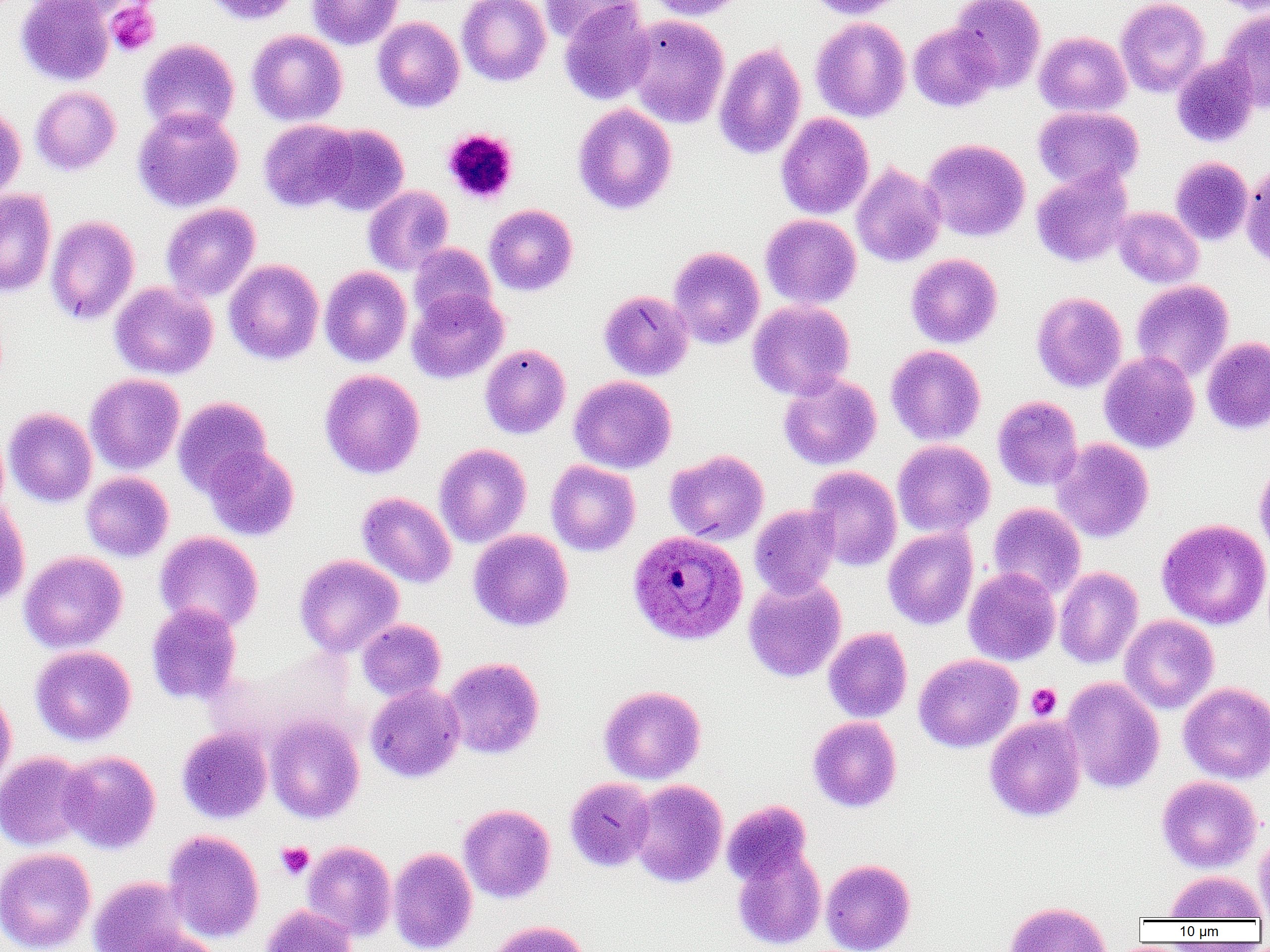 Approximate bounding boxes as (x1, y1, x2, y2) in pixels. Plasmodium ovale-infected red blood cell locations: (627, 529, 748, 645). Platelet locations (subset): (442, 128, 519, 204), (1026, 683, 1061, 720), (276, 842, 314, 879). Uninfected red blood cell locations (subset): (16, 0, 114, 86), (27, 0, 141, 22), (200, 0, 301, 25), (307, 0, 403, 50), (457, 0, 551, 86), (541, 0, 638, 44), (643, 0, 748, 21), (806, 0, 908, 19), (949, 0, 1046, 92), (1115, 0, 1210, 97), (1209, 0, 1270, 14), (559, 1, 654, 106), (1217, 8, 1270, 111), (624, 14, 729, 128), (372, 17, 465, 112), (810, 17, 911, 122), (908, 23, 998, 112), (247, 29, 347, 126), (1034, 31, 1132, 117), (138, 38, 240, 135), (714, 43, 807, 160), (1171, 55, 1261, 148), (30, 86, 121, 176), (0, 103, 26, 202), (573, 103, 677, 215), (1033, 106, 1143, 192), (133, 107, 243, 212), (775, 113, 874, 219), (258, 119, 358, 212), (312, 123, 409, 215), (922, 139, 1030, 242), (1170, 156, 1253, 246), (1241, 161, 1270, 271), (851, 162, 946, 268), (1031, 167, 1133, 267), (363, 185, 454, 276), (0, 189, 56, 298), (161, 203, 260, 302), (484, 204, 578, 295), (1113, 207, 1203, 288), (760, 214, 862, 309), (45, 215, 140, 325), (408, 243, 497, 326), (668, 246, 765, 349), (906, 253, 1003, 348), (224, 259, 324, 365), (320, 266, 412, 366), (1131, 280, 1234, 381), (110, 282, 218, 379), (407, 289, 509, 384), (598, 290, 694, 381), (1031, 292, 1127, 393), (747, 300, 855, 400), (1202, 337, 1270, 434), (480, 343, 571, 439), (886, 345, 986, 445), (1099, 352, 1200, 453), (319, 369, 425, 479), (85, 373, 185, 475), (778, 373, 882, 470), (569, 375, 677, 473), (992, 395, 1083, 491), (173, 396, 273, 496), (3, 407, 97, 508), (892, 439, 995, 538), (1051, 439, 1154, 543), (434, 444, 531, 548), (202, 445, 300, 541), (665, 449, 769, 545), (1254, 458, 1270, 562), (546, 460, 641, 556), (806, 466, 902, 570), (81, 472, 173, 561), (357, 492, 456, 588), (0, 499, 30, 607), (987, 502, 1086, 599), (749, 504, 840, 598), (1157, 519, 1270, 630), (883, 526, 978, 630), (468, 529, 574, 631), (154, 531, 264, 633), (19, 551, 127, 653), (294, 554, 403, 658), (1054, 566, 1143, 669), (963, 568, 1060, 665), (743, 576, 846, 682), (146, 602, 243, 706), (1120, 614, 1219, 713), (357, 619, 446, 701), (823, 627, 912, 722), (30, 645, 136, 746), (913, 653, 1023, 753), (442, 657, 545, 759), (1060, 677, 1165, 794), (1178, 681, 1270, 783), (365, 683, 466, 783), (0, 685, 16, 792), (598, 685, 706, 784), (265, 715, 364, 823), (807, 716, 902, 813), (985, 716, 1086, 821), (177, 726, 273, 824), (58, 750, 161, 853), (0, 751, 93, 851), (1157, 775, 1262, 872), (565, 777, 655, 871), (627, 779, 728, 888), (722, 800, 813, 887), (458, 804, 555, 903), (1254, 826, 1270, 921), (163, 829, 264, 942), (302, 840, 397, 941), (732, 845, 826, 950), (0, 847, 96, 952), (388, 847, 477, 952), (821, 858, 915, 952), (1164, 870, 1268, 920), (87, 876, 205, 952), (1004, 901, 1112, 952), (259, 904, 358, 952), (485, 920, 589, 952). Slide-level diagnosis: Plasmodium ovale. 1000x magnification. Image is 1270×952 pixels. Single field of view. Thin blood smear. Optical microscopy.